Classify this cell by malaria status.
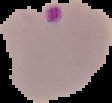
Parasitized.

From a thin blood smear. Cell region segmented out of the field of view; the surrounding area is masked to black. Image is 112×103 pixels.